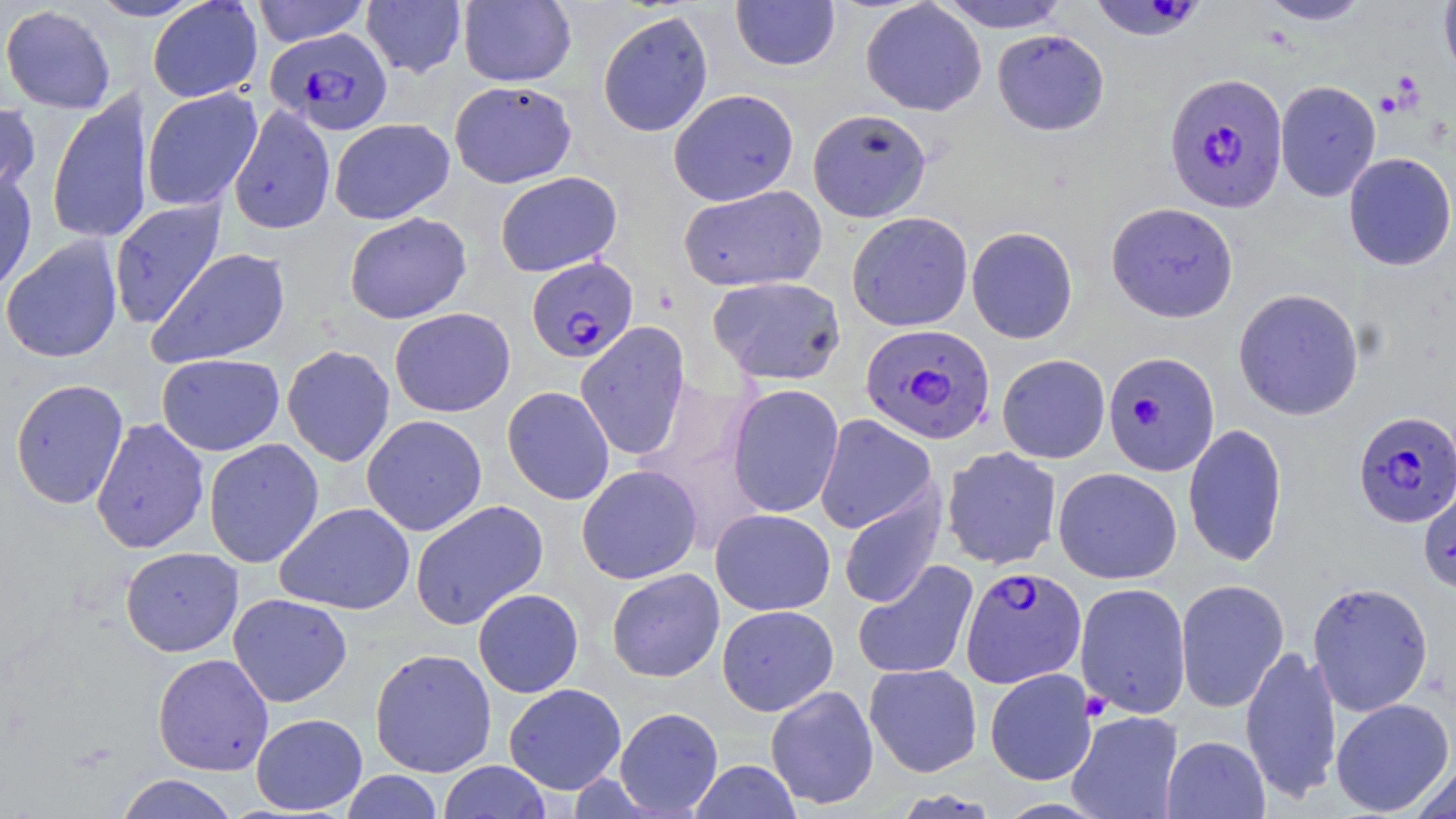

Approximate bounding boxes as [x1, y1, x2, y2] in pixels. Plasmodium falciparum-infected red blood cell locations: [1086, 1, 1209, 42], [265, 28, 392, 134], [1164, 73, 1288, 212], [526, 256, 638, 363], [860, 324, 995, 445], [1102, 351, 1220, 476], [1353, 410, 1456, 527], [961, 566, 1086, 687]. Uninfected red blood cell locations: [86, 0, 208, 21], [147, 0, 263, 103], [935, 0, 1073, 33], [1256, 0, 1372, 25], [251, 1, 371, 46], [362, 1, 467, 78], [458, 1, 576, 87], [731, 1, 840, 71], [860, 1, 986, 116], [1439, 1, 1456, 84], [0, 4, 117, 113], [597, 10, 714, 137], [992, 29, 1110, 136], [449, 80, 577, 188], [1275, 80, 1381, 201], [45, 87, 153, 247], [141, 87, 263, 212], [668, 88, 799, 206], [0, 98, 41, 202], [228, 105, 336, 235], [807, 108, 931, 222], [329, 118, 455, 224], [1343, 153, 1456, 271], [0, 166, 38, 296], [495, 171, 622, 277], [678, 185, 827, 292], [108, 199, 227, 329], [1106, 202, 1239, 323], [344, 211, 472, 324], [846, 211, 973, 332], [966, 226, 1078, 344], [1, 236, 123, 364], [148, 248, 292, 368], [707, 276, 847, 385], [1233, 288, 1364, 420], [389, 307, 515, 417], [575, 321, 691, 461], [282, 345, 395, 467], [157, 353, 285, 456], [997, 354, 1110, 463], [10, 378, 129, 509], [727, 383, 844, 518], [502, 386, 614, 505], [361, 414, 487, 536], [814, 414, 936, 534], [90, 417, 210, 555], [1183, 423, 1288, 566], [204, 438, 324, 568], [941, 446, 1062, 570], [576, 464, 703, 584], [1053, 467, 1182, 584], [1418, 486, 1456, 595], [838, 488, 946, 609], [409, 500, 548, 630], [275, 502, 415, 614], [710, 508, 835, 615], [120, 547, 243, 656], [852, 559, 979, 680], [607, 568, 725, 682], [1175, 578, 1289, 713], [1307, 581, 1434, 716], [1075, 582, 1191, 719], [473, 588, 584, 697], [228, 593, 352, 707], [717, 605, 839, 716], [1240, 644, 1342, 804], [369, 648, 497, 778], [152, 653, 273, 776], [864, 663, 982, 777], [984, 668, 1097, 785], [503, 683, 626, 795], [765, 684, 879, 810], [1331, 698, 1454, 816], [614, 706, 724, 816], [1066, 710, 1184, 819], [251, 713, 368, 815], [1161, 735, 1270, 819], [1410, 759, 1456, 819], [439, 760, 552, 819], [689, 760, 802, 819], [341, 770, 442, 819], [114, 773, 240, 819]. Platelet locations: [1376, 91, 1403, 117], [1080, 691, 1112, 720]. Slide-level diagnosis: Plasmodium falciparum. Optical microscopy. 1000x magnification. May-Grünwald-Giemsa stain. Thin blood smear. Image is 1456×819 pixels. Single field of view.